Identify the preparation type.
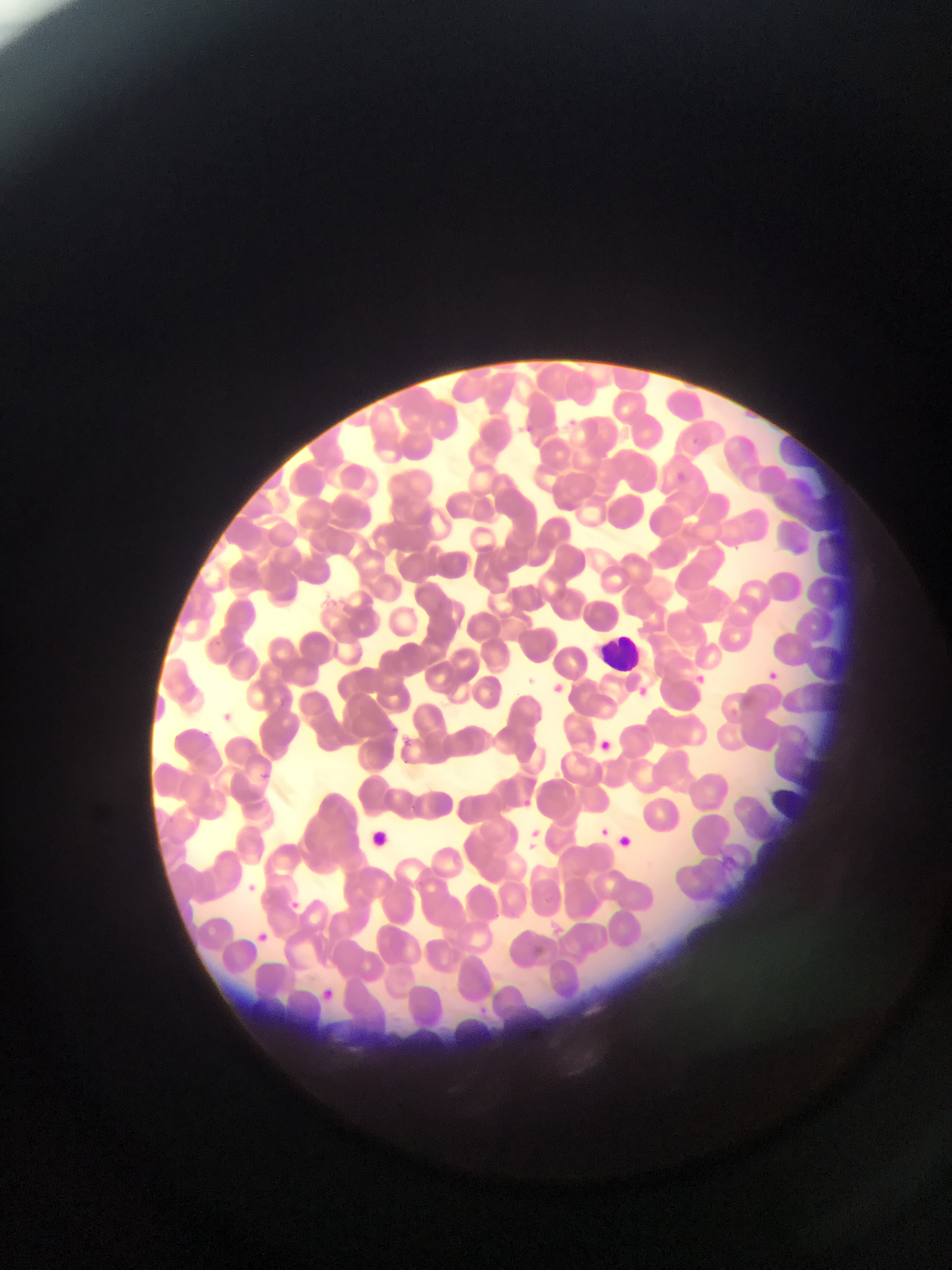
Thin blood smear.

field of view = single
leukocyte locations = approximate bounding boxes as [left, top, right, bottom] in pixels: [594, 632, 650, 678], [768, 776, 806, 834]
country = Ghana
Plasmodium parasite locations = approximate bounding boxes as [left, top, right, bottom] in pixels: [565, 414, 585, 429], [522, 422, 534, 435], [692, 436, 705, 450], [674, 470, 689, 480], [767, 668, 778, 680], [696, 673, 711, 687], [552, 681, 565, 698], [635, 685, 652, 700], [217, 708, 233, 721], [386, 725, 405, 735], [404, 734, 415, 749], [601, 736, 612, 752], [259, 763, 278, 780], [523, 796, 536, 807], [601, 824, 617, 841], [530, 825, 553, 840], [529, 842, 538, 853], [246, 884, 261, 894], [292, 900, 306, 912], [258, 932, 272, 942], [482, 1003, 492, 1016]
image size = 952×1270 pixels
capture = mobile-phone photograph through a microscope